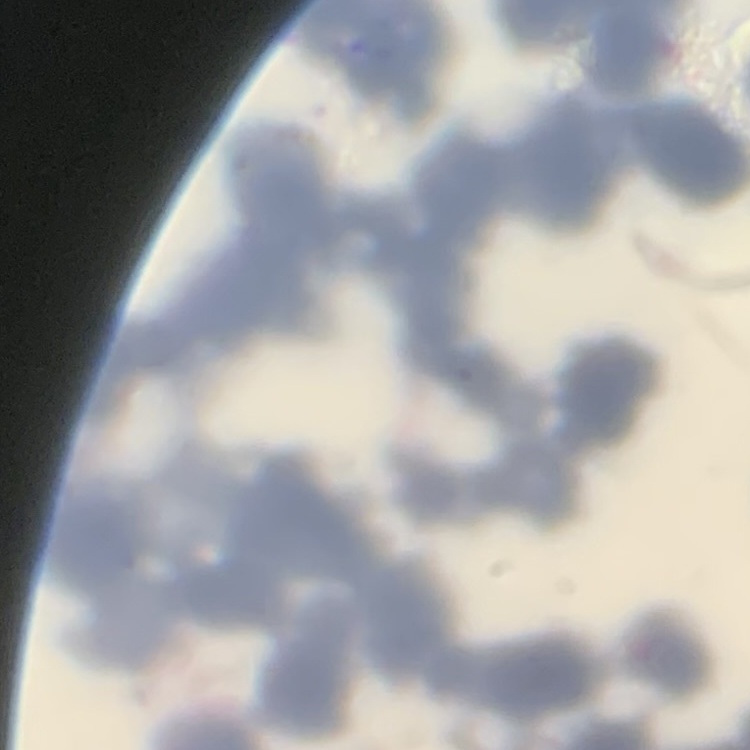
red blood cell morphology = rouleaux formation
stain = Field's or Giemsa
image type = square crop of a larger photomicrograph
preparation = thin blood smear